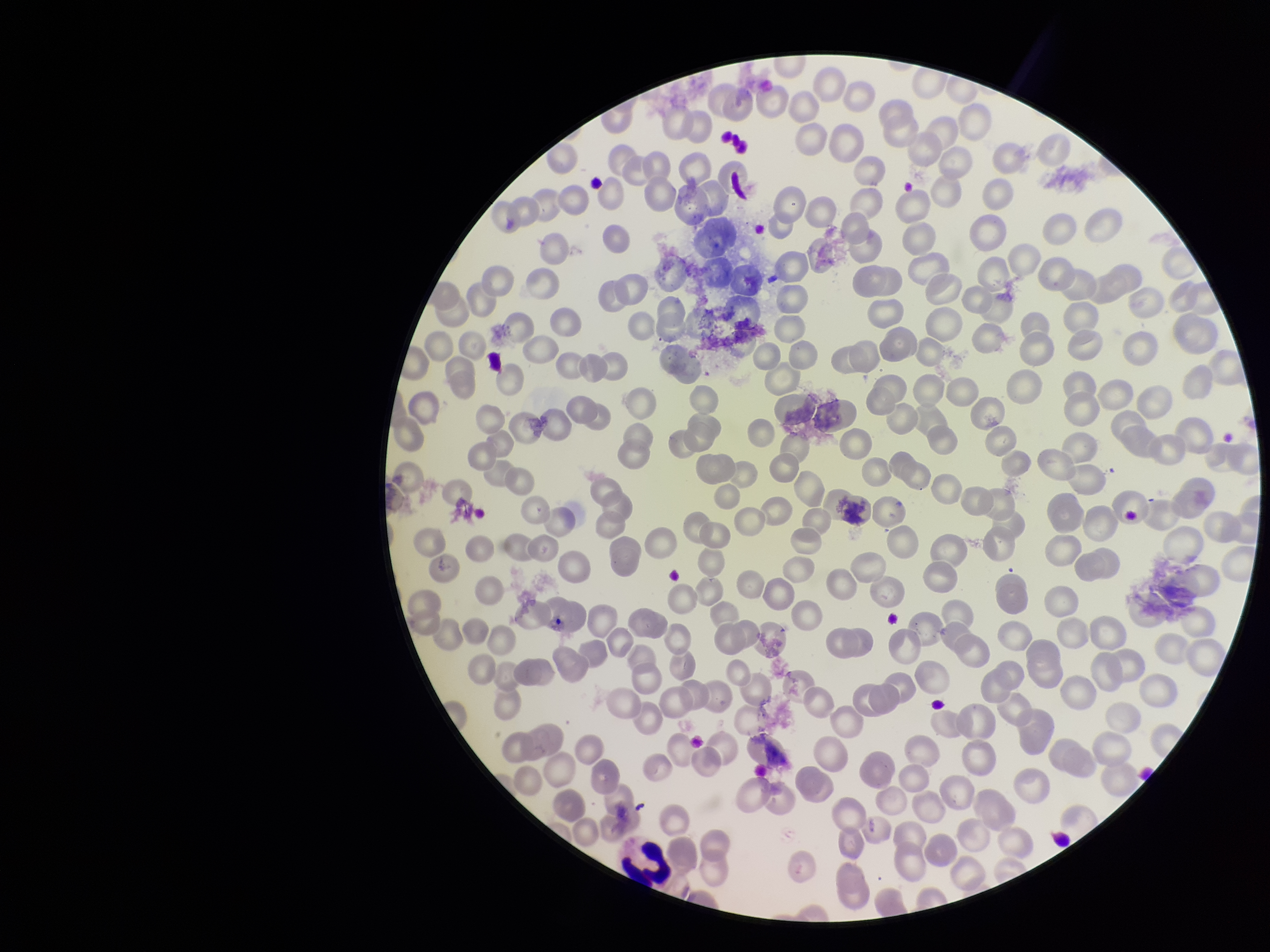

parasitized red blood cell count = 0
parasitized red blood cells = none detected
patient malaria status = infected
stain = Giemsa
red blood cell count = 241
capture = smartphone photograph through the microscope eyepiece
image size = 1270×952 pixels
field of view = one from this slide
species reported for this patient = Plasmodium vivax
preparation = thin